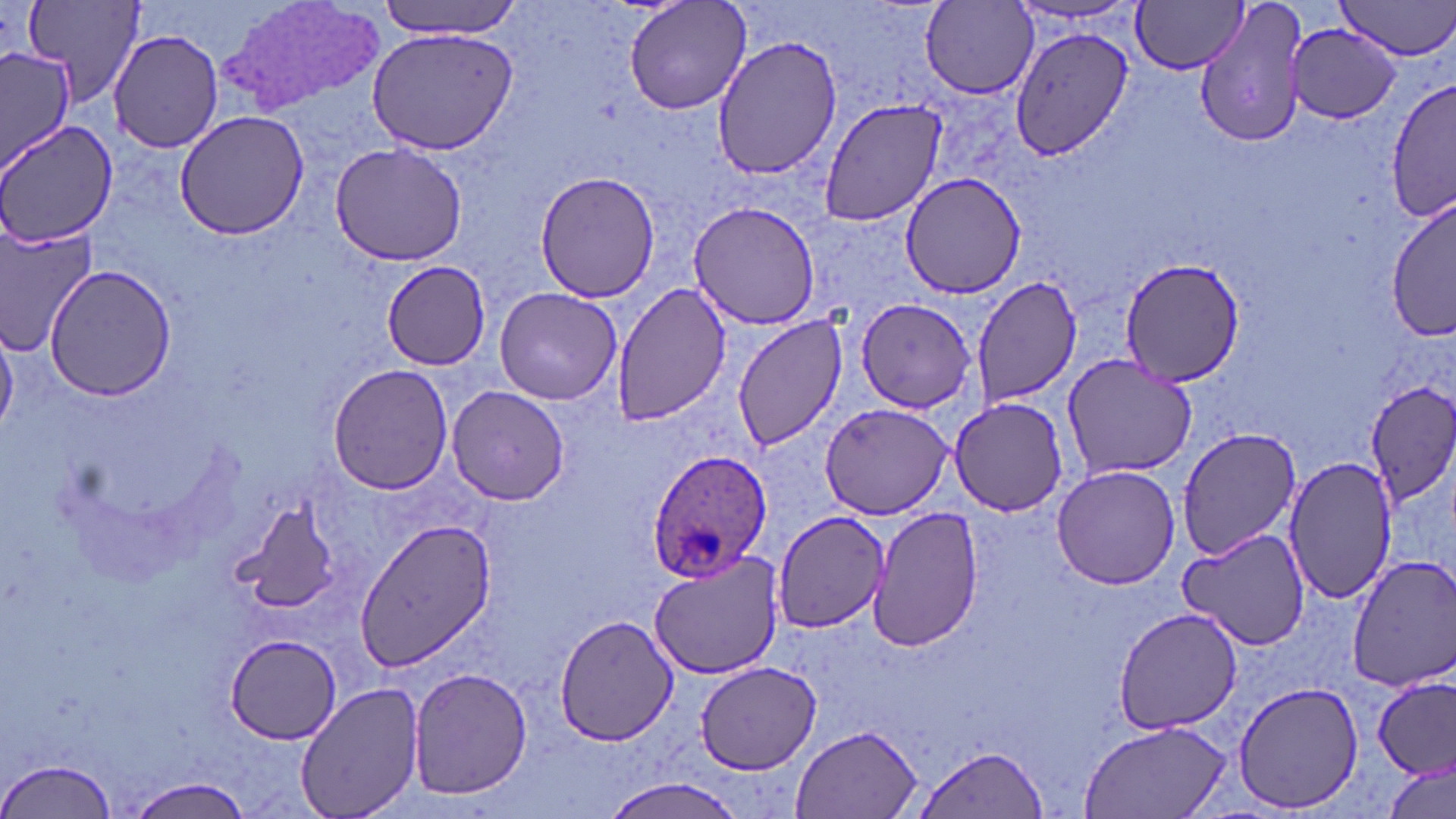
Summary:
  - Coordinate format: approximate bounding boxes as named x1/y1/x2/y2 corners in pixels
  - Uninfected red blood cell locations: (x1=24, y1=0, x2=148, y2=108), (x1=373, y1=0, x2=526, y2=40), (x1=623, y1=0, x2=752, y2=117), (x1=1133, y1=0, x2=1249, y2=74), (x1=1194, y1=0, x2=1311, y2=150), (x1=1335, y1=0, x2=1456, y2=60), (x1=918, y1=1, x2=1040, y2=100), (x1=1009, y1=22, x2=1133, y2=161), (x1=1286, y1=23, x2=1401, y2=123), (x1=364, y1=25, x2=519, y2=155), (x1=108, y1=28, x2=225, y2=154), (x1=712, y1=35, x2=844, y2=182), (x1=0, y1=46, x2=75, y2=174), (x1=1385, y1=75, x2=1456, y2=225), (x1=817, y1=97, x2=947, y2=228), (x1=174, y1=109, x2=308, y2=240), (x1=0, y1=119, x2=117, y2=249), (x1=330, y1=140, x2=467, y2=267), (x1=534, y1=169, x2=661, y2=302), (x1=900, y1=173, x2=1025, y2=299), (x1=1389, y1=201, x2=1456, y2=343), (x1=687, y1=202, x2=820, y2=330), (x1=0, y1=225, x2=98, y2=351), (x1=1121, y1=259, x2=1245, y2=386), (x1=383, y1=260, x2=492, y2=368), (x1=46, y1=266, x2=176, y2=400), (x1=970, y1=273, x2=1083, y2=408), (x1=607, y1=280, x2=732, y2=425), (x1=492, y1=285, x2=622, y2=404), (x1=855, y1=297, x2=978, y2=415), (x1=731, y1=314, x2=846, y2=453), (x1=1061, y1=355, x2=1198, y2=480), (x1=327, y1=364, x2=451, y2=495), (x1=1364, y1=382, x2=1456, y2=514), (x1=445, y1=385, x2=570, y2=504), (x1=946, y1=397, x2=1070, y2=516), (x1=818, y1=400, x2=956, y2=519), (x1=1176, y1=425, x2=1306, y2=557), (x1=1283, y1=455, x2=1394, y2=604), (x1=1050, y1=464, x2=1180, y2=590), (x1=228, y1=500, x2=345, y2=614), (x1=866, y1=505, x2=985, y2=653), (x1=773, y1=511, x2=890, y2=632), (x1=352, y1=517, x2=497, y2=675), (x1=1178, y1=526, x2=1309, y2=650), (x1=649, y1=550, x2=782, y2=681), (x1=1348, y1=555, x2=1456, y2=692), (x1=1112, y1=606, x2=1243, y2=734), (x1=556, y1=613, x2=678, y2=746), (x1=227, y1=634, x2=345, y2=745), (x1=695, y1=661, x2=820, y2=774), (x1=407, y1=667, x2=531, y2=798), (x1=1375, y1=678, x2=1455, y2=783), (x1=296, y1=679, x2=425, y2=819), (x1=1234, y1=679, x2=1364, y2=814), (x1=1078, y1=719, x2=1233, y2=819), (x1=790, y1=723, x2=924, y2=819), (x1=914, y1=745, x2=1050, y2=817), (x1=2, y1=755, x2=121, y2=819), (x1=1382, y1=760, x2=1454, y2=819), (x1=126, y1=774, x2=254, y2=817), (x1=598, y1=777, x2=748, y2=818)
  - Plasmodium ovale-infected red blood cell locations: (x1=646, y1=452, x2=775, y2=579)
  - Slide-level diagnosis: Plasmodium ovale
  - Modality: light microscopy
  - Stain: May-Grünwald-Giemsa
  - Image size: 1456×819 pixels
  - Preparation: thin blood film
  - Field of view: single
  - Magnification: 1000x